Report the malaria status of this cell.
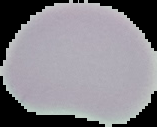
Uninfected.

From a thin blood smear. Segmented cell region on a black background. Image is 157×127 pixels.